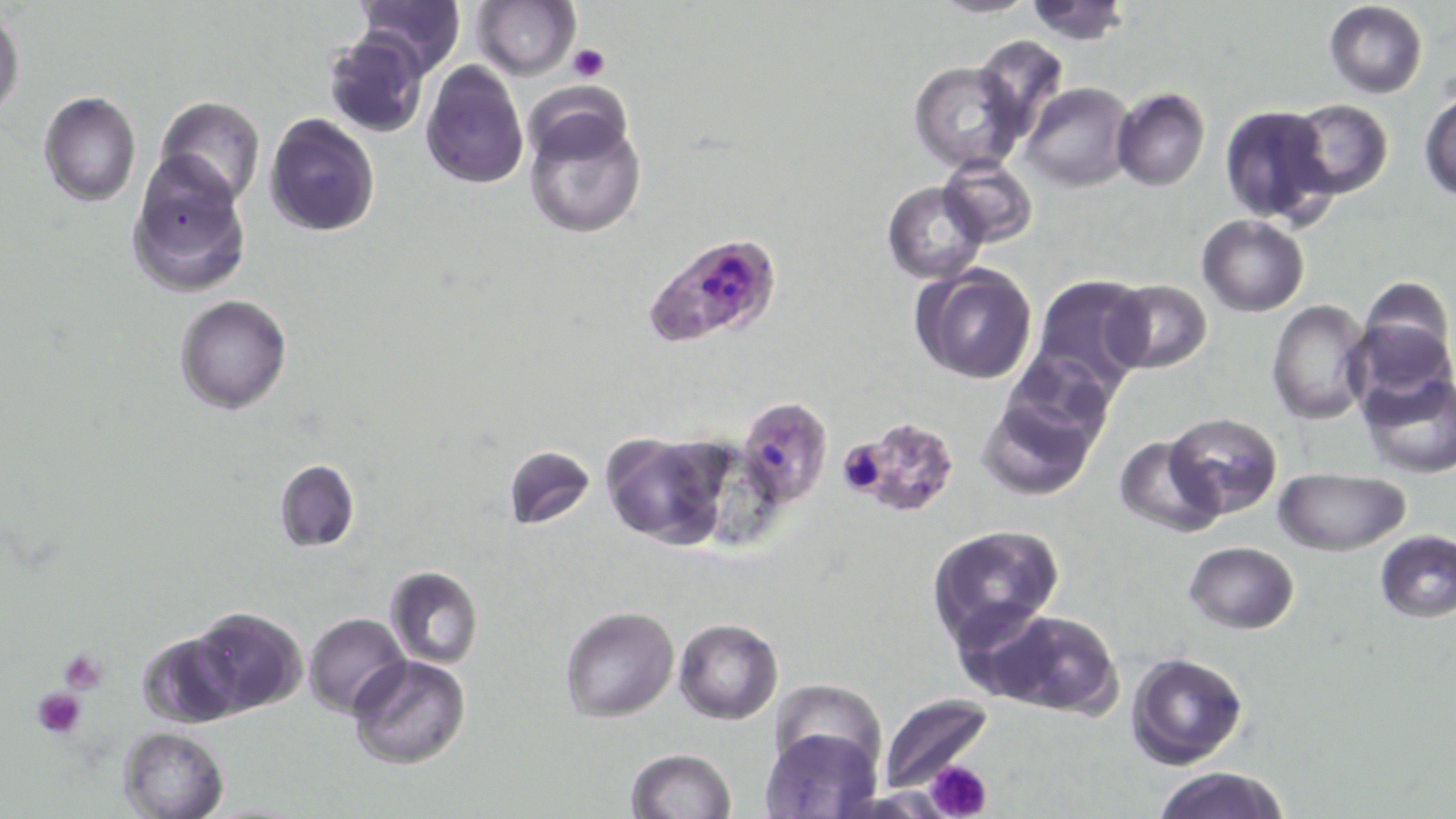
Approximate bounding boxes as (x1,y1)-(x2,y2) corner pairs in pixels. Platelet locations: (568,43)-(609,83), (59,649)-(109,693), (32,686)-(89,736), (929,760)-(993,819). Uninfected red blood cell locations: (351,0)-(467,77), (472,0)-(579,79), (929,0)-(1040,17), (1021,0)-(1132,44), (1323,2)-(1428,98), (0,13)-(25,118), (323,31)-(428,138), (974,33)-(1070,147), (910,61)-(1026,173), (422,62)-(529,188), (1021,82)-(1133,192), (1112,87)-(1210,191), (1421,92)-(1456,200), (38,93)-(143,207), (156,96)-(264,202), (1282,99)-(1393,200), (523,103)-(647,240), (1217,103)-(1336,227), (266,115)-(380,238), (126,153)-(251,298), (937,156)-(1038,248), (883,181)-(987,283), (1198,214)-(1309,315), (912,264)-(1039,385), (1030,275)-(1150,399), (1356,277)-(1455,388), (1105,280)-(1213,373), (174,294)-(292,414), (1266,300)-(1372,424), (1357,370)-(1456,480), (976,389)-(1101,500), (735,395)-(833,508), (1164,412)-(1282,518), (599,429)-(731,549), (1112,433)-(1223,538), (505,444)-(595,531), (274,459)-(358,552), (1273,468)-(1411,555), (926,524)-(1063,645), (1375,531)-(1456,623), (1184,542)-(1299,633), (384,566)-(483,669), (185,605)-(309,716), (560,606)-(680,722), (977,609)-(1121,715), (303,613)-(410,716), (673,617)-(783,723), (136,630)-(243,730), (1126,651)-(1250,771), (347,655)-(472,771), (766,679)-(884,772), (877,694)-(992,794), (118,726)-(229,819), (760,726)-(878,818), (626,746)-(737,819), (1151,765)-(1290,819). Plasmodium falciparum-infected red blood cell locations: (642,233)-(780,350), (842,417)-(958,517). Slide-level diagnosis: Plasmodium falciparum. Thin blood smear. Captured at 1000x magnification. Optical microscopy. One field of a larger specimen. Image is 1456×819 pixels. May-Grünwald-Giemsa stain.